Evaluate for malaria.
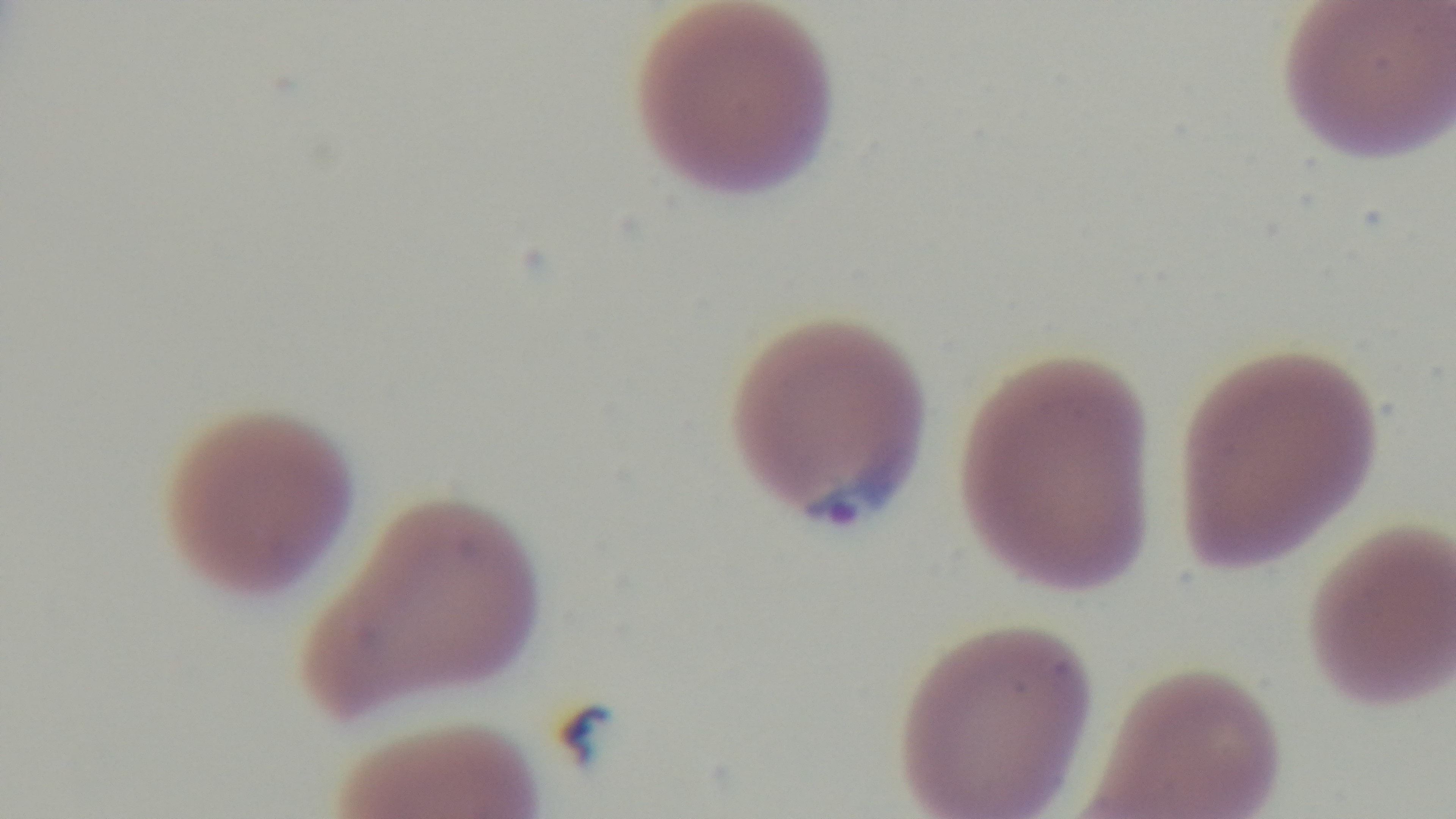

It is infected.

{
  "modality": "light microscopy",
  "objective": "100x oil immersion",
  "preparation": "thin blood film",
  "stain": "Giemsa",
  "capture": "mounted 4K digital camera",
  "field_of_view": "one from the slide"
}